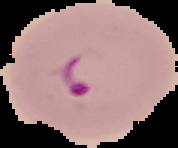
Summary:
  - Result: Plasmodium parasites detected
  - Preparation: thin blood smear
  - Image size: 178×148 pixels
  - Image type: segmented cell region on a black background